Describe the morphology of the red blood cells.
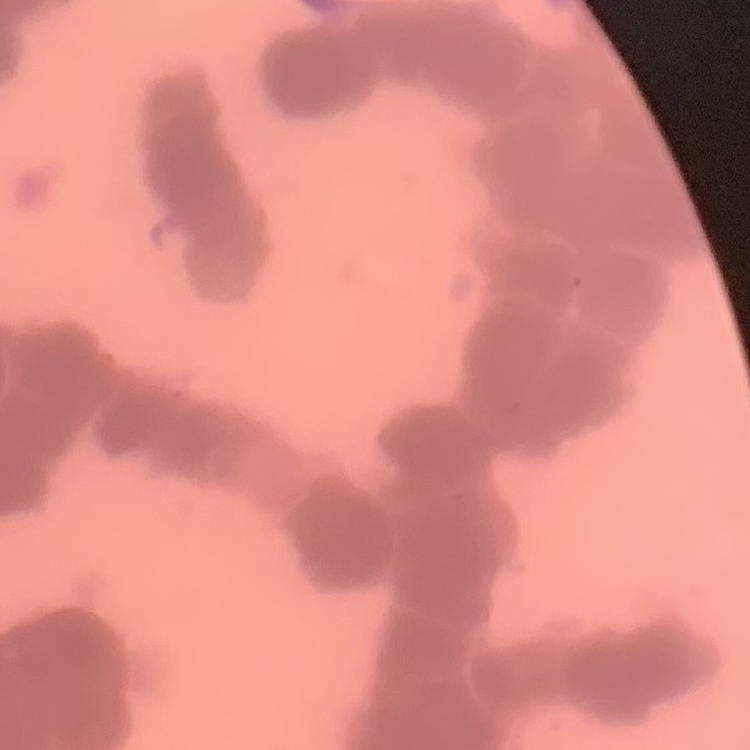
They show rouleaux formation.

stain = Field's or Giemsa
image type = square crop of a larger photomicrograph
preparation = thin peripheral smear